Outline each blood parasite and name the species.
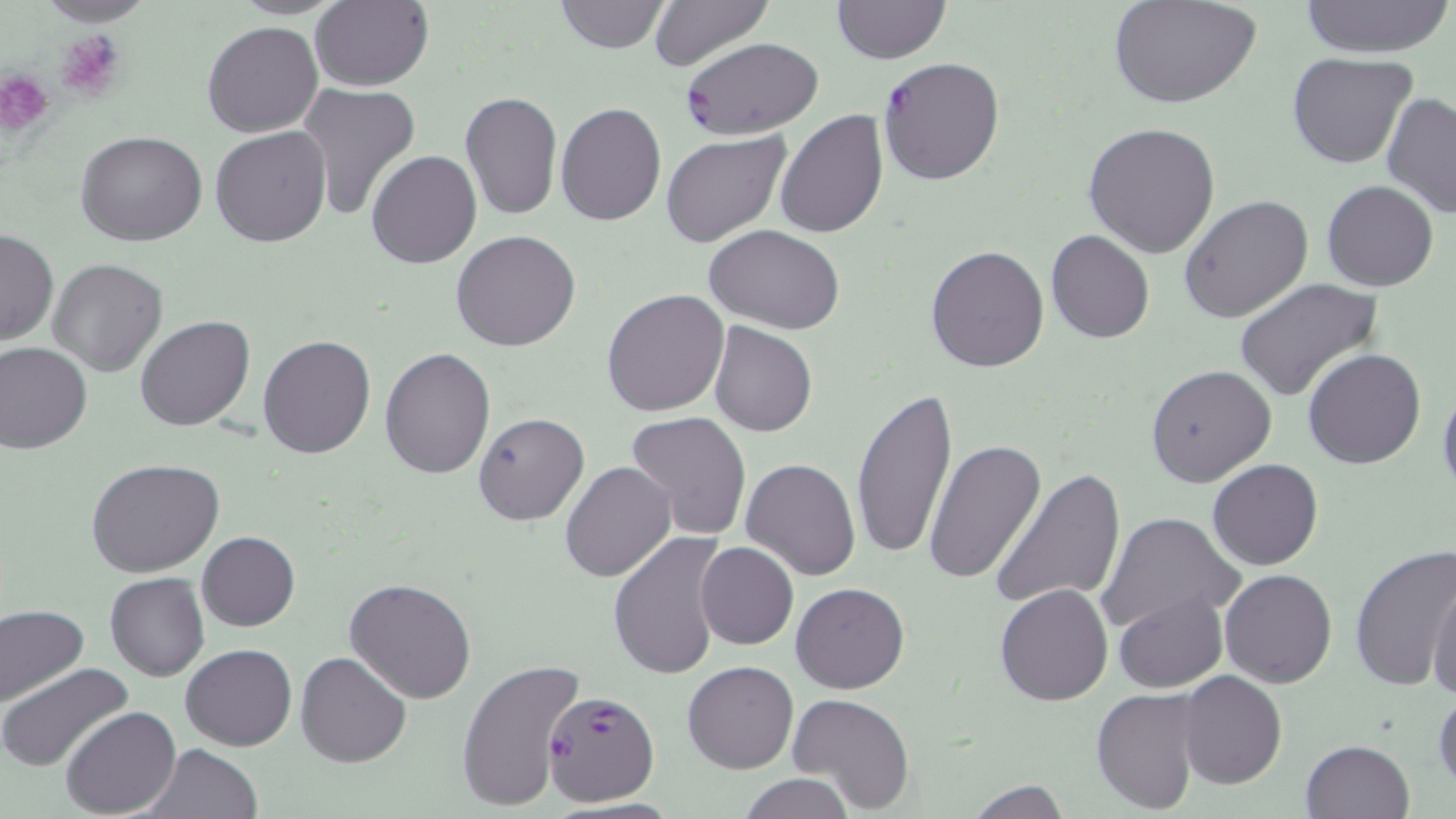
Approximate bounding boxes as named x1/y1/x2/y2 corners in pixels.
Plasmodium falciparum-infected red blood cells: (x1=679, y1=37, x2=825, y2=139), (x1=876, y1=57, x2=1006, y2=187), (x1=540, y1=688, x2=660, y2=807).
No Plasmodium ovale, Plasmodium malariae, Plasmodium vivax, Babesia divergens, or Trypanosoma brucei observed.

slide-level diagnosis = Plasmodium falciparum
magnification = 1000x
preparation = thin blood smear
platelet locations = approximate bounding boxes as named x1/y1/x2/y2 corners in pixels: (x1=56, y1=34, x2=124, y2=97), (x1=1, y1=72, x2=50, y2=134)
stain = May-Grünwald-Giemsa
field of view = single
modality = light microscopy
image size = 1456×819 pixels
uninfected red blood cell locations = approximate bounding boxes as named x1/y1/x2/y2 corners in pixels: (x1=34, y1=0, x2=158, y2=26), (x1=226, y1=0, x2=349, y2=18), (x1=310, y1=0, x2=435, y2=92), (x1=553, y1=0, x2=672, y2=54), (x1=649, y1=0, x2=774, y2=70), (x1=832, y1=0, x2=949, y2=64), (x1=1296, y1=0, x2=1452, y2=57), (x1=1109, y1=1, x2=1257, y2=109), (x1=202, y1=20, x2=324, y2=137), (x1=1288, y1=53, x2=1420, y2=171), (x1=295, y1=81, x2=422, y2=223), (x1=460, y1=91, x2=562, y2=220), (x1=1382, y1=93, x2=1456, y2=219), (x1=555, y1=102, x2=666, y2=225), (x1=774, y1=109, x2=888, y2=240), (x1=1083, y1=122, x2=1220, y2=259), (x1=209, y1=128, x2=331, y2=246), (x1=76, y1=129, x2=207, y2=245), (x1=660, y1=131, x2=790, y2=248), (x1=367, y1=150, x2=481, y2=269), (x1=1321, y1=180, x2=1438, y2=291), (x1=1180, y1=193, x2=1314, y2=323), (x1=704, y1=225, x2=846, y2=332), (x1=0, y1=229, x2=58, y2=346), (x1=450, y1=229, x2=581, y2=352), (x1=1046, y1=231, x2=1154, y2=344), (x1=925, y1=243, x2=1050, y2=373), (x1=47, y1=258, x2=168, y2=376), (x1=1234, y1=276, x2=1385, y2=404), (x1=602, y1=288, x2=729, y2=416), (x1=134, y1=315, x2=256, y2=431), (x1=709, y1=321, x2=817, y2=436), (x1=258, y1=335, x2=377, y2=458), (x1=0, y1=342, x2=93, y2=454), (x1=380, y1=346, x2=495, y2=479), (x1=1303, y1=349, x2=1425, y2=469), (x1=1146, y1=363, x2=1276, y2=486), (x1=1437, y1=379, x2=1456, y2=498), (x1=850, y1=387, x2=957, y2=561), (x1=624, y1=411, x2=753, y2=540), (x1=473, y1=412, x2=589, y2=525), (x1=924, y1=439, x2=1046, y2=583), (x1=85, y1=457, x2=226, y2=577), (x1=740, y1=457, x2=862, y2=580), (x1=1207, y1=458, x2=1323, y2=571), (x1=559, y1=460, x2=677, y2=583), (x1=990, y1=467, x2=1126, y2=611), (x1=1096, y1=511, x2=1243, y2=634), (x1=197, y1=531, x2=300, y2=631), (x1=609, y1=531, x2=726, y2=680), (x1=696, y1=541, x2=798, y2=649), (x1=1350, y1=545, x2=1456, y2=693), (x1=1220, y1=569, x2=1337, y2=688), (x1=106, y1=572, x2=209, y2=681), (x1=1429, y1=574, x2=1456, y2=702), (x1=345, y1=577, x2=477, y2=704), (x1=792, y1=581, x2=909, y2=693), (x1=995, y1=584, x2=1113, y2=706), (x1=1113, y1=591, x2=1225, y2=693), (x1=0, y1=604, x2=88, y2=708), (x1=181, y1=643, x2=297, y2=751), (x1=295, y1=650, x2=411, y2=768), (x1=457, y1=659, x2=585, y2=813), (x1=682, y1=660, x2=798, y2=773), (x1=0, y1=662, x2=132, y2=771), (x1=1176, y1=670, x2=1287, y2=789), (x1=1433, y1=682, x2=1455, y2=793), (x1=1091, y1=688, x2=1207, y2=814), (x1=787, y1=692, x2=915, y2=814), (x1=61, y1=706, x2=179, y2=817), (x1=1300, y1=739, x2=1416, y2=819), (x1=143, y1=744, x2=262, y2=818), (x1=737, y1=775, x2=856, y2=818), (x1=965, y1=779, x2=1072, y2=818)